Identify the cell.
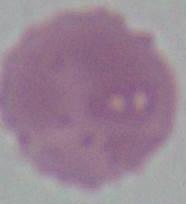
An erythrocyte.

magnification = 1000x
modality = micrograph